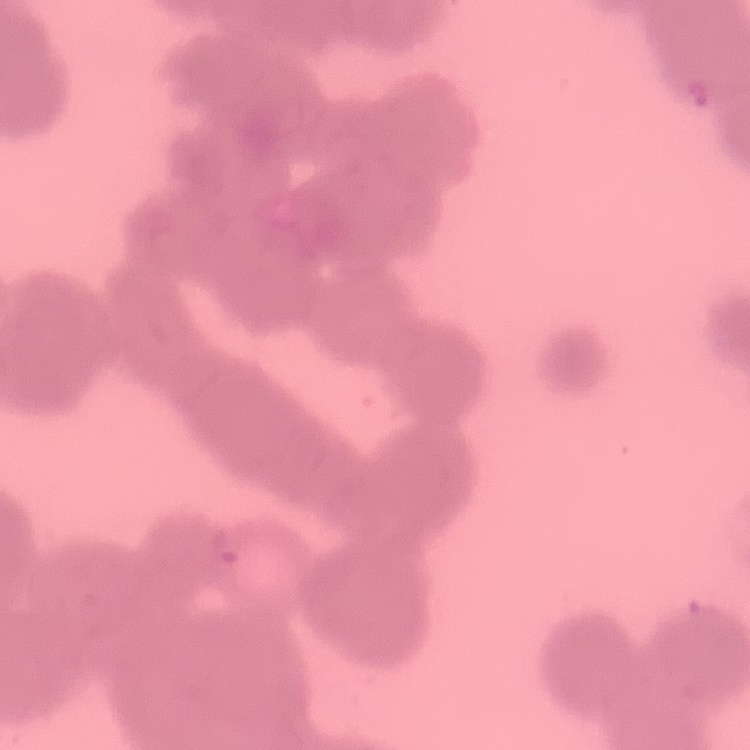
Summary:
  - Erythrocyte morphology: rouleaux formation
  - Preparation: thin peripheral smear
  - Stain: Field's or Giemsa
  - Image type: one tile cut from a larger photomicrograph